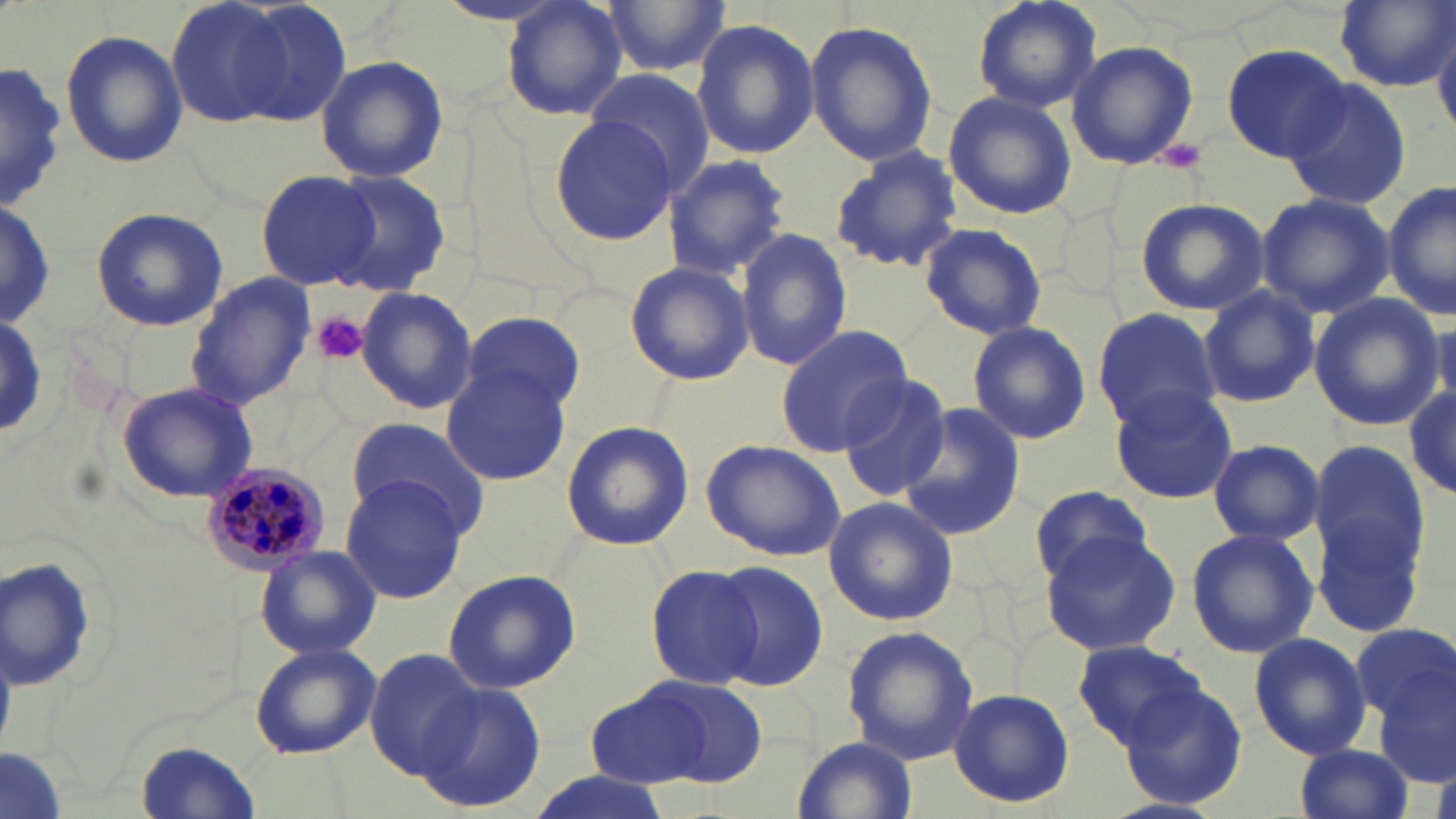
Approximate bounding boxes as (x1,y1)-(x2,y2) corner pairs in pixels. Plasmodium malariae-infected red blood cell locations: (198,460)-(329,575). Platelet locations: (1154,138)-(1206,174), (314,313)-(367,364). Uninfected red blood cell locations: (971,0)-(1104,113), (166,1)-(302,129), (229,1)-(355,126), (502,1)-(630,121), (601,1)-(730,78), (1332,1)-(1452,92), (804,18)-(938,166), (690,19)-(820,160), (1432,19)-(1456,140), (59,29)-(187,169), (1065,40)-(1200,170), (1221,42)-(1352,162), (315,55)-(448,183), (0,59)-(67,215), (581,69)-(717,195), (1281,81)-(1413,212), (943,91)-(1076,219), (545,110)-(678,247), (828,146)-(966,274), (661,154)-(793,279), (255,169)-(377,290), (324,171)-(451,297), (1384,181)-(1455,323), (1256,192)-(1394,319), (0,195)-(53,336), (1133,198)-(1269,315), (89,205)-(228,331), (919,222)-(1049,341), (735,228)-(852,370), (623,260)-(754,386), (185,273)-(318,411), (1198,285)-(1319,409), (356,286)-(478,415), (1307,294)-(1443,430), (1092,307)-(1220,430), (460,311)-(584,416), (0,312)-(47,440), (966,321)-(1091,446), (776,324)-(915,454), (441,361)-(572,487), (835,374)-(954,502), (115,382)-(259,503), (1107,385)-(1238,505), (354,386)-(564,506), (1406,389)-(1456,499), (896,404)-(1027,541), (346,416)-(485,533), (559,420)-(693,551), (700,438)-(846,563), (1207,439)-(1324,547), (1311,440)-(1428,569), (341,474)-(470,604), (1027,485)-(1155,587), (822,496)-(959,628), (1310,510)-(1430,643), (1039,526)-(1178,655), (1185,528)-(1317,659), (255,546)-(381,660), (2,553)-(100,691), (643,562)-(768,689), (710,562)-(829,689), (443,567)-(583,693), (1349,623)-(1454,725), (841,626)-(979,765), (1247,633)-(1372,760), (1072,642)-(1208,750), (250,643)-(381,758), (365,649)-(481,778), (1372,667)-(1455,784), (640,676)-(771,786), (1110,676)-(1249,812), (414,679)-(546,811), (585,681)-(718,788), (948,687)-(1075,810), (794,733)-(916,819), (134,738)-(262,818), (1295,741)-(1414,819), (0,747)-(67,819), (519,773)-(675,819). Slide-level diagnosis: Plasmodium malariae. May-Grünwald-Giemsa-stained preparation. Thin blood film. Image is 1456×819 pixels. 1000x magnification. Optical microscopy. Single field of view.